Report the malaria status of this cell.
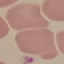

Uninfected.

Giemsa-stained preparation. Cell patch, automatically extracted from a larger field of view and resized to 64 × 64 pixels. Photographed with a smartphone camera at the microscope eyepiece. Thin blood film.